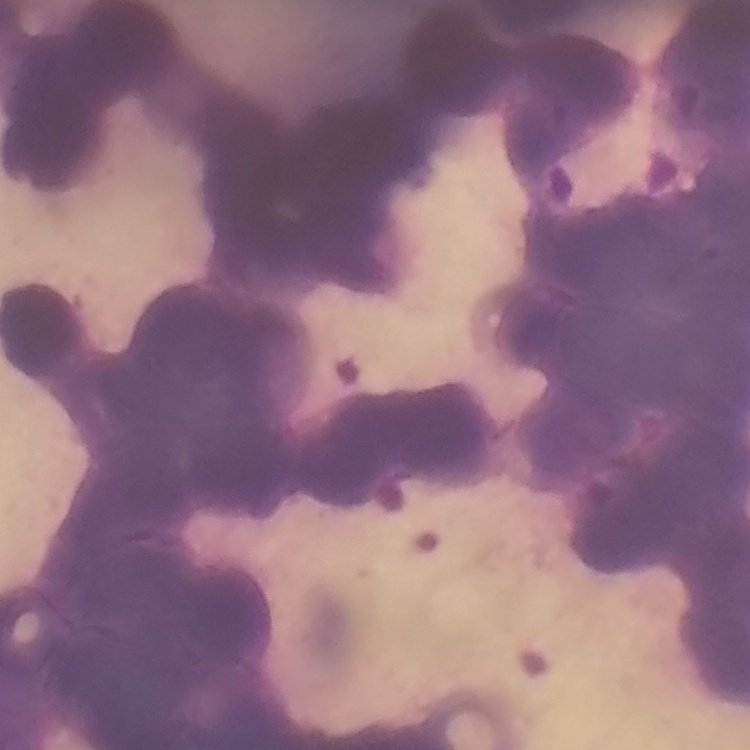

Summary:
  - Red blood cell morphology: rouleaux formation
  - Image type: one tile cut from a larger photomicrograph
  - Preparation: thin peripheral smear
  - Stain: Field's or Giemsa